State the preparation type.
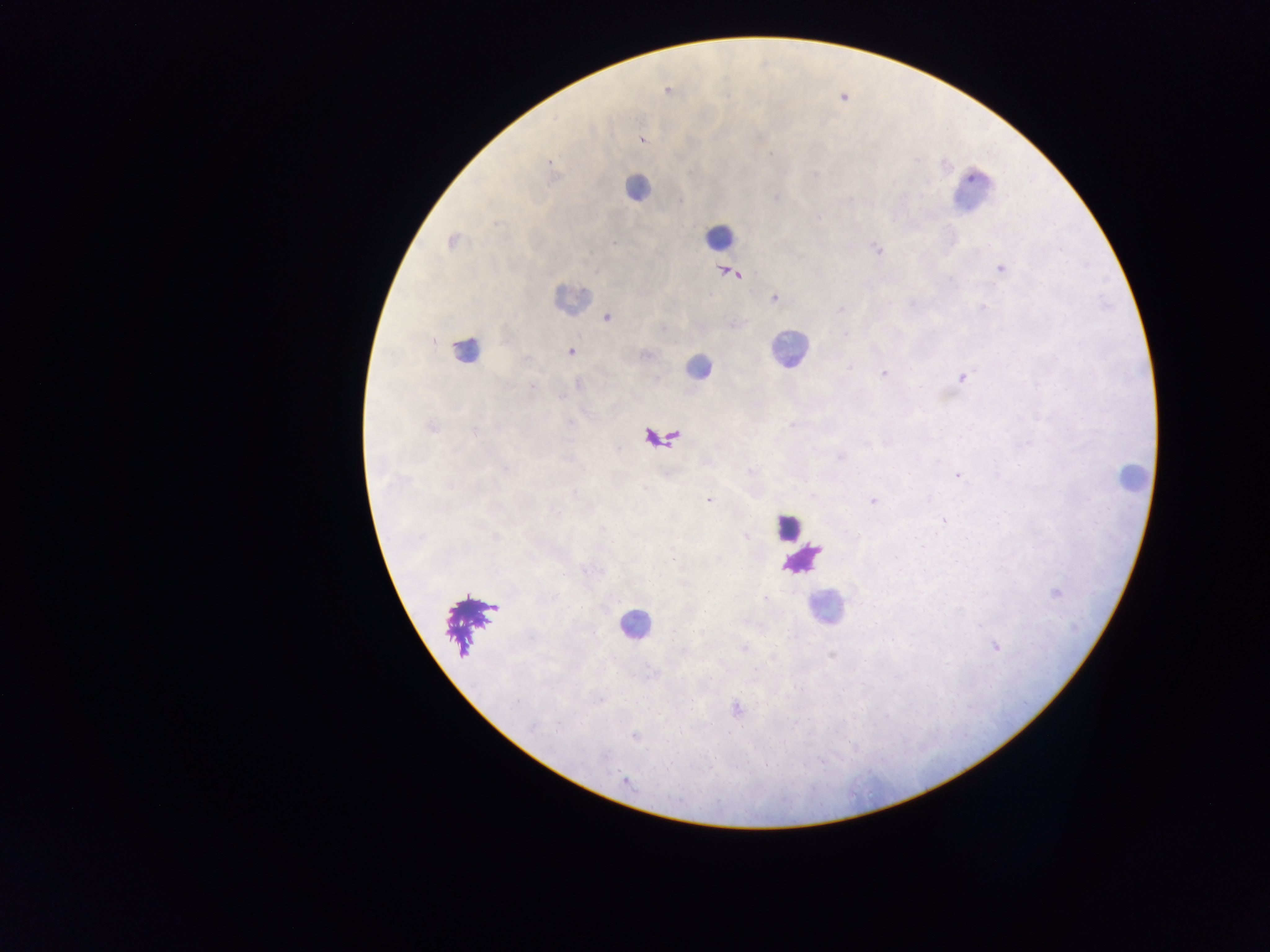

Thick blood film.

country = Ghana
malaria parasite locations = approximate centers as {x, y} in pixels: {668, 90}, {641, 139}, {549, 162}, {452, 241}, {877, 249}, {1000, 268}, {729, 272}, {773, 297}, {607, 318}, {571, 352}, {884, 374}, {962, 376}, {432, 427}, {957, 475}, {813, 495}, {709, 501}, {873, 501}, {1056, 592}, {995, 646}, {735, 708}, {765, 765}, {626, 781}
leukocyte locations = approximate centers as {x, y} in pixels: {637, 187}, {971, 192}, {718, 237}, {571, 298}, {789, 349}, {465, 350}, {696, 367}, {661, 439}, {1130, 477}, {789, 527}, {803, 559}, {826, 607}, {471, 624}, {634, 626}
image size = 1270×952 pixels
field of view = single
capture = mobile-phone photograph through a microscope